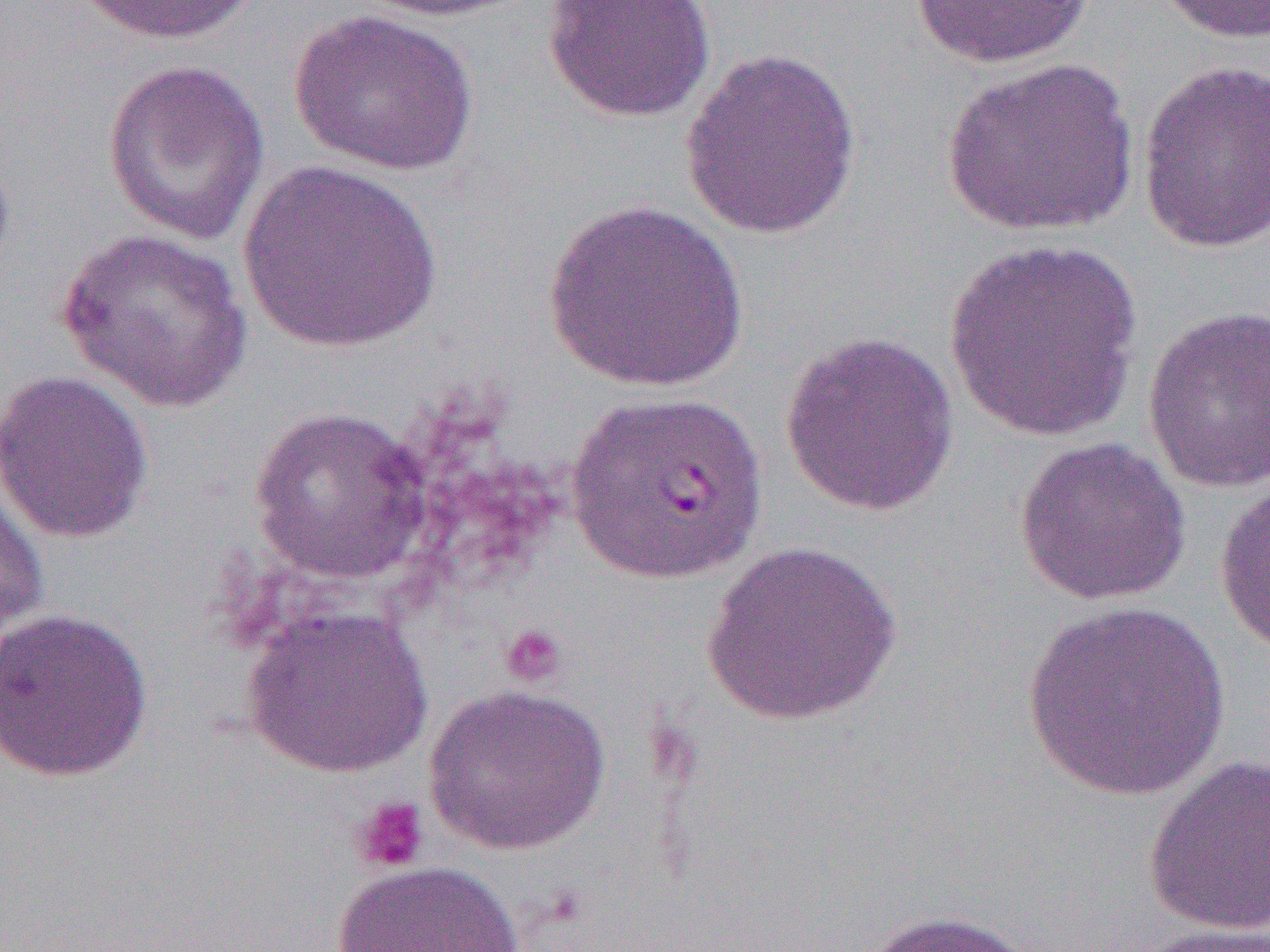

Approximate bounding boxes as (x1,y1)-(x2,y2) corner pairs in pixels. Uninfected red blood cell locations: (71,0)-(262,46), (352,0)-(531,22), (541,0)-(717,123), (909,0)-(1097,69), (1153,0)-(1270,44), (289,8)-(479,176), (679,45)-(862,240), (941,57)-(1140,237), (101,58)-(271,246), (1137,59)-(1270,255), (238,159)-(443,355), (542,199)-(748,393), (56,227)-(254,415), (943,240)-(1144,443), (1142,305)-(1270,495), (779,330)-(959,516), (0,370)-(154,544), (565,388)-(768,585), (250,406)-(431,585), (1013,435)-(1192,606), (0,479)-(48,646), (1214,481)-(1270,656), (704,542)-(904,726), (1019,601)-(1232,802), (241,606)-(432,778), (0,607)-(154,783), (423,683)-(611,856), (1142,755)-(1270,937), (332,860)-(524,952), (858,909)-(1035,952), (1128,923)-(1270,952). Platelet locations: (499,624)-(567,688), (350,795)-(430,874). Slide-level diagnosis: Plasmodium falciparum. Optical microscopy. Single field of view. 1000x magnification. Image is 1270×952 pixels. Thin blood smear.